Assess this cell for malaria.
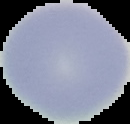

Uninfected.

image size = 130×124 pixels
preparation = thin blood film
image type = segmented cell region with the area outside set to black